Report the malaria status of this cell.
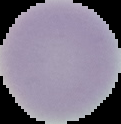

Uninfected.

Image is 121×124 pixels. The area outside the segmented cell region is set to black. From a thin blood film.